Locate every Plasmodium parasite.
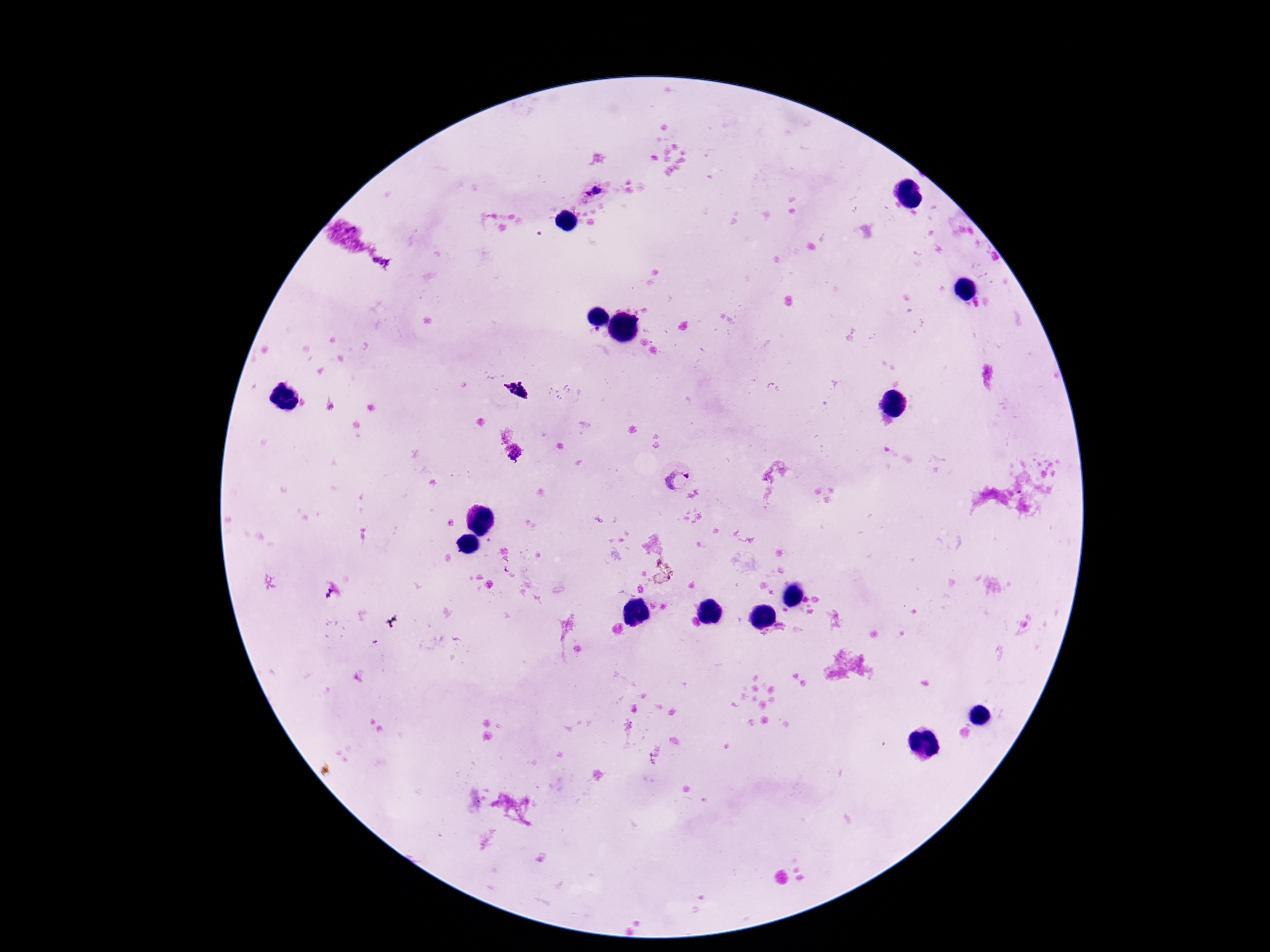

Approximate object centers, in pixels from the top-left corner.
Plasmodium parasites: (x=591, y=191), (x=516, y=390), (x=676, y=475).

{
  "magnification": "100x",
  "image_size": "1270×952 pixels",
  "preparation": "thick blood smear",
  "patient_malaria_status": "infected",
  "field_of_view": "single",
  "capture": "smartphone camera through the microscope eyepiece",
  "stain": "Giemsa"
}